Assess this cell for malaria.
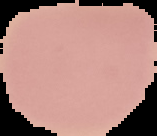

It is uninfected.

Segmented cell region on a black background. Image is 157×136 pixels. From a thin blood smear.